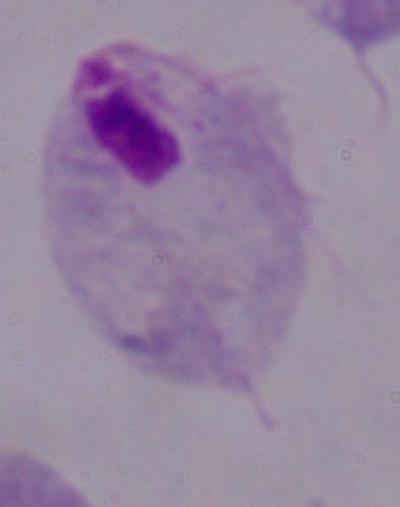 A trichomonad is seen. Captured at 1000x magnification. Photomicrograph.